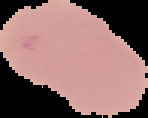 Malaria status: uninfected. Image is 148×118 pixels. The area outside the segmented cell region is set to black. From a thin blood smear.